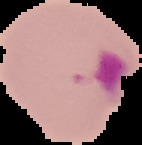
Summary:
  - Preparation: thin blood film
  - Image size: 142×145 pixels
  - Image type: cell region segmented out of the field of view; surrounding area masked to black
  - Malaria status: parasitized